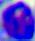
A leukocyte is shown. Captured at 400x magnification. Micrograph.